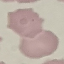 Malaria status: uninfected. Acquired by smartphone through the microscope eyepiece. Thin blood film. Automatically extracted cell patch, resized to 64 × 64 pixels. Giemsa stain.